Assess this cell for malaria.
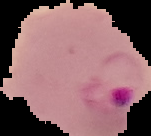
It is parasitized.

From a thin blood smear. Image is 151×136 pixels. Segmented cell region on a black background.